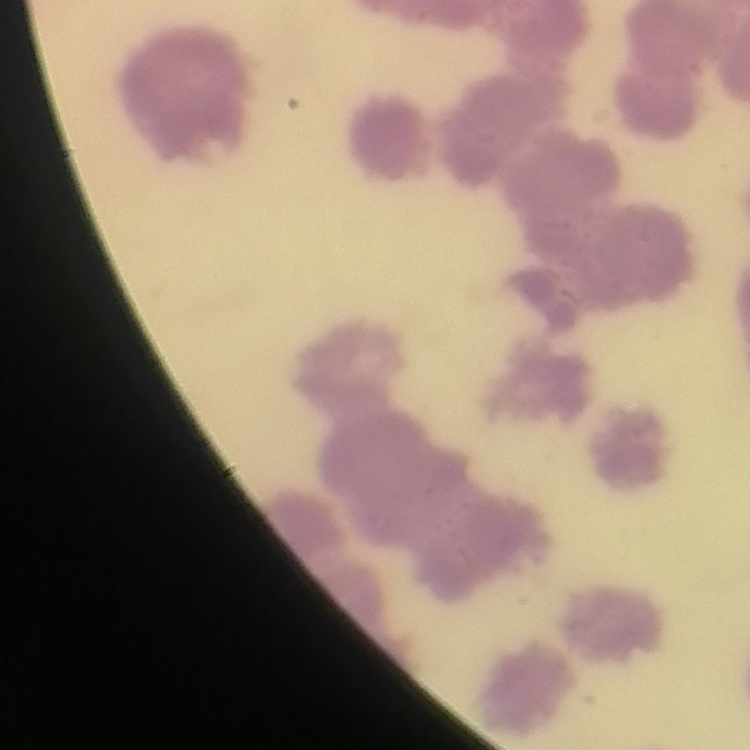

The red blood cells exhibit rouleaux formation. Thin blood smear. Stained with either Field's or Giemsa. Square crop of a larger photomicrograph.